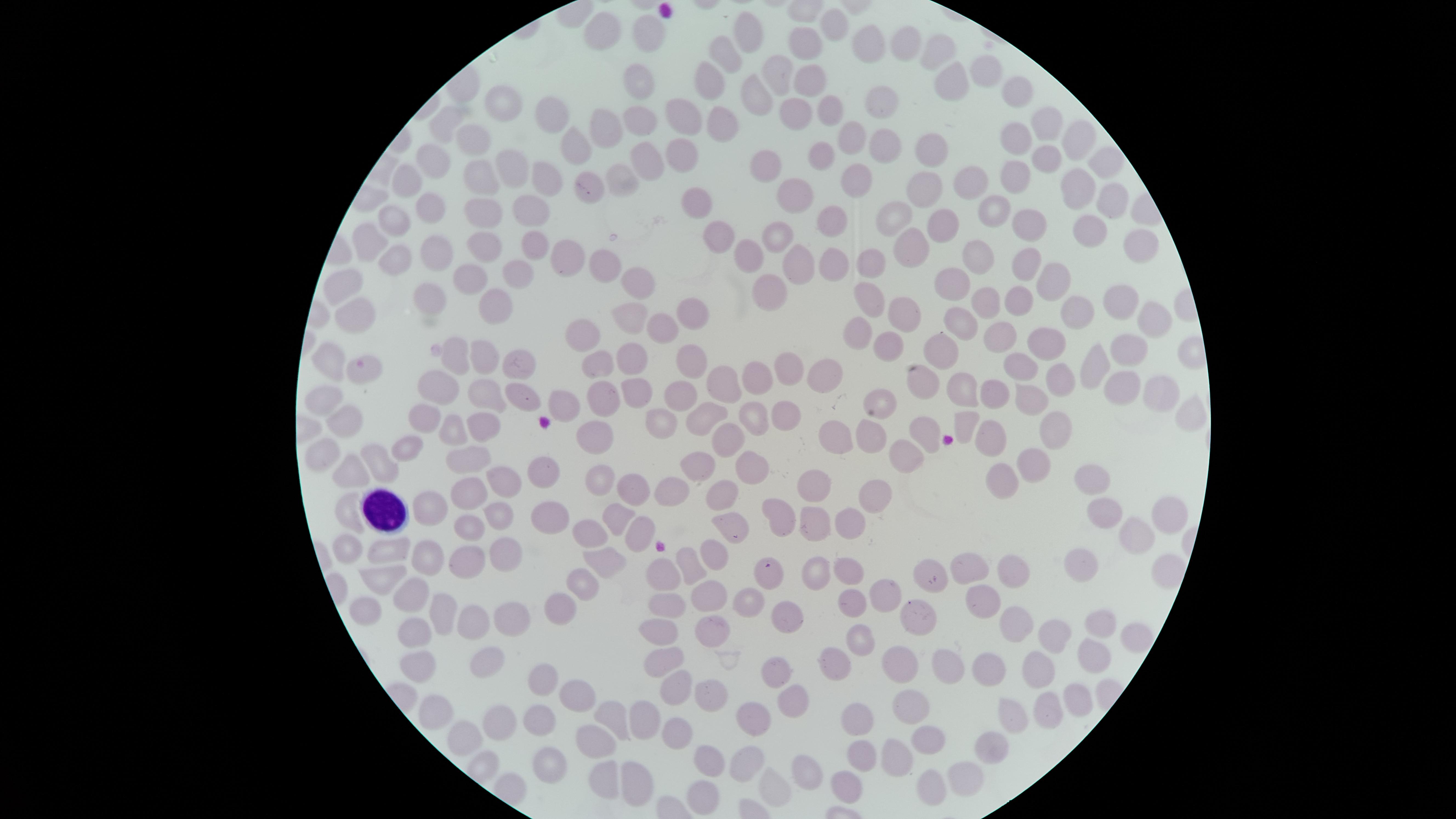
Approximate marker points as [x, y] in pixels.
Summary:
  - Uninfected RBCs: [832, 24], [599, 29], [748, 35], [650, 36], [800, 38], [903, 38], [867, 39], [942, 51], [727, 54], [770, 69], [980, 72], [805, 73], [710, 80], [951, 80], [636, 81], [748, 88], [1015, 92], [505, 106], [821, 106], [874, 106], [794, 115], [685, 117], [549, 118], [633, 120], [449, 122], [722, 122], [1052, 123], [602, 127], [474, 135], [1014, 136], [855, 137], [1080, 139], [574, 143], [885, 148], [927, 149], [824, 153], [1045, 156], [682, 158], [1106, 158], [434, 159], [512, 160], [641, 163], [762, 165], [477, 174], [1016, 174], [407, 175], [616, 175], [542, 177], [855, 177], [960, 179], [588, 182], [920, 186], [1080, 187], [801, 189], [1104, 199], [700, 202], [991, 204], [426, 205], [532, 209], [488, 213], [895, 213], [833, 215], [393, 216], [938, 224], [1027, 228], [1093, 230], [779, 238], [369, 239], [718, 239], [529, 242], [486, 244], [1132, 245], [910, 247], [745, 250], [556, 252], [430, 253], [987, 255], [397, 257], [872, 259], [834, 260], [1026, 262], [597, 263], [800, 264], [516, 275], [467, 279], [1054, 279], [955, 281], [627, 282], [770, 283], [347, 286], [428, 287], [870, 299], [984, 299], [1113, 299], [1019, 302], [493, 304], [900, 312], [1086, 312], [690, 313], [623, 315], [359, 317], [964, 318], [1148, 319], [667, 325], [861, 330], [1055, 332], [582, 334], [1002, 334], [888, 343], [1125, 346], [484, 348], [942, 353], [694, 355], [451, 360], [628, 361], [329, 362], [516, 362], [598, 366], [1021, 366], [1095, 368], [359, 369], [789, 369], [825, 372], [757, 373], [1064, 376], [921, 378], [438, 384], [720, 385], [1128, 386], [482, 387], [1156, 387], [955, 388], [994, 388], [637, 391], [523, 392], [678, 393], [325, 397], [593, 399], [881, 400], [1031, 400], [563, 405], [423, 410], [781, 412], [706, 417], [751, 417], [1192, 417], [345, 418], [661, 418], [485, 420], [966, 420], [446, 428], [1056, 429], [869, 430], [919, 430], [837, 432], [594, 433], [991, 434], [730, 435], [407, 441], [473, 457], [902, 458], [320, 461], [382, 462], [750, 464], [695, 467], [355, 471], [1032, 471], [548, 473], [508, 479], [597, 480], [816, 482], [1001, 482], [1089, 483], [632, 484], [670, 488], [465, 491], [725, 491], [877, 500], [432, 503], [349, 505], [551, 513], [780, 514], [1102, 514], [494, 519], [614, 519], [819, 519], [1162, 519], [856, 524], [463, 525], [633, 528], [728, 529], [591, 534], [1134, 535], [343, 547], [399, 547], [503, 550], [431, 556], [715, 556], [1087, 560], [599, 561], [467, 563], [688, 567], [813, 567], [968, 568], [844, 569], [1009, 570], [933, 571], [383, 573], [1164, 573], [663, 575], [770, 575], [583, 587], [882, 592], [408, 593], [709, 594], [741, 598], [668, 600], [979, 600], [853, 602], [560, 604], [361, 609], [438, 610], [788, 610], [918, 613], [506, 619], [1019, 620], [1098, 621], [475, 623], [663, 626], [707, 630], [1050, 631], [416, 636], [1134, 640], [859, 641], [1093, 653], [488, 656], [673, 659], [897, 660], [940, 663], [828, 664], [418, 668], [776, 668], [982, 669], [1038, 673], [544, 680], [673, 683], [708, 696], [574, 699], [789, 699], [1072, 704], [913, 706], [1040, 708], [436, 712], [614, 715], [750, 715], [1007, 715], [650, 716], [542, 718], [859, 720], [502, 724], [675, 729], [462, 735], [925, 737], [598, 741], [987, 746], [862, 754], [895, 756], [749, 759], [707, 761], [547, 768], [807, 769], [599, 776], [965, 777], [634, 780], [846, 785], [930, 786], [775, 787], [701, 799]
  - WBCs: [386, 511]
  - Presence: no malaria parasites detected
  - Field of view: single
  - Capture: smartphone photograph through the microscope eyepiece
  - Stain: Giemsa
  - Visible region: circular
  - Preparation: thin blood smear
  - Image size: 1456×819 pixels